Locate every Plasmodium parasite and every leukocyte.
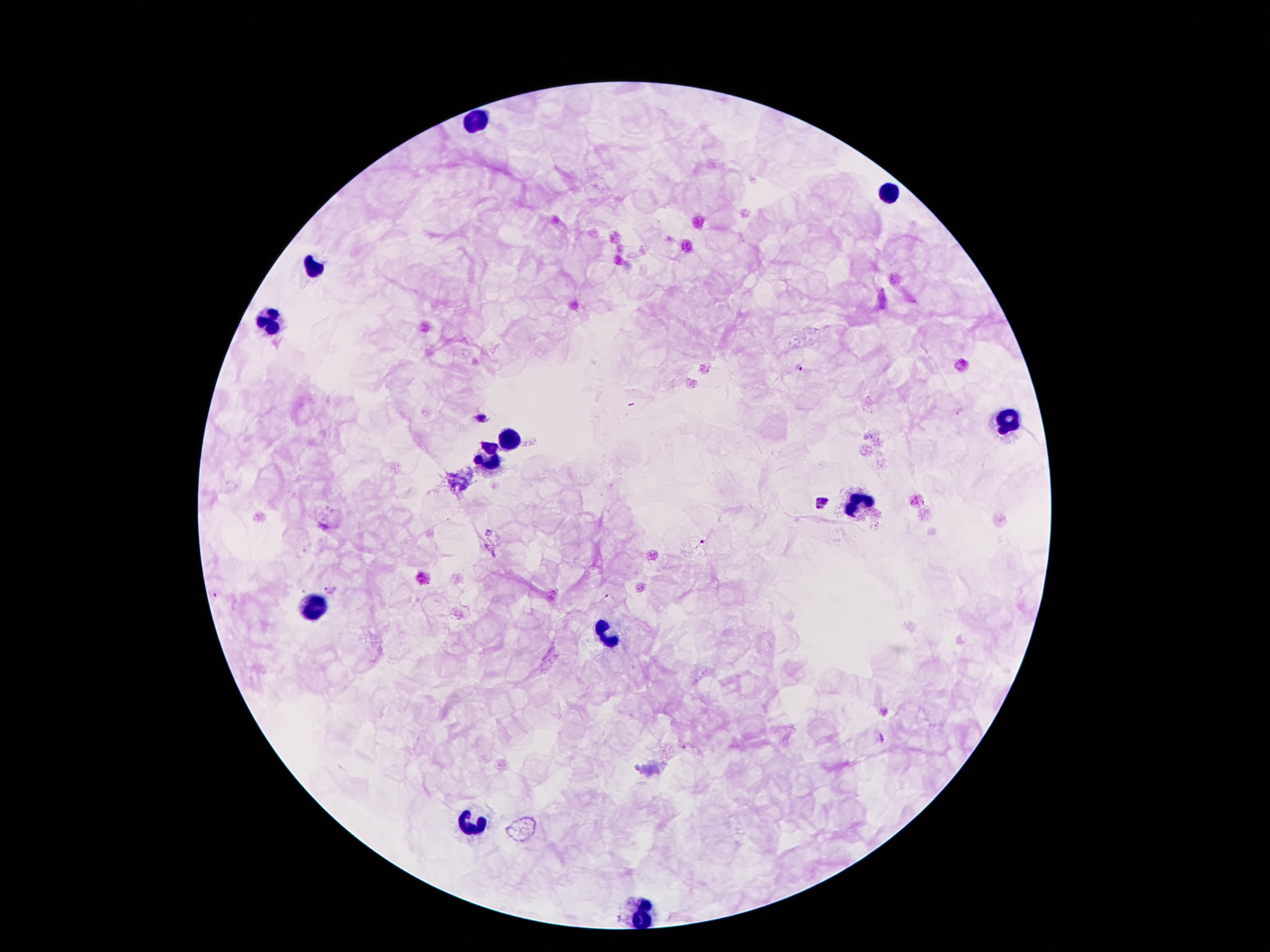

Approximate centers as [x, y] in pixels.
Plasmodium parasites: [798, 367], [482, 417], [822, 501], [703, 543], [332, 590].
Leukocytes: [473, 121], [885, 189], [315, 270], [273, 319], [1010, 420], [508, 443], [490, 458], [859, 503], [312, 607], [609, 636], [472, 827], [646, 904], [640, 921].

capture: smartphone camera through the microscope eyepiece
patient_malaria_status: positive for Plasmodium falciparum
stain: Giemsa
preparation: thick blood smear
image_size: 1270×952 pixels
field_of_view: single
magnification: 100x